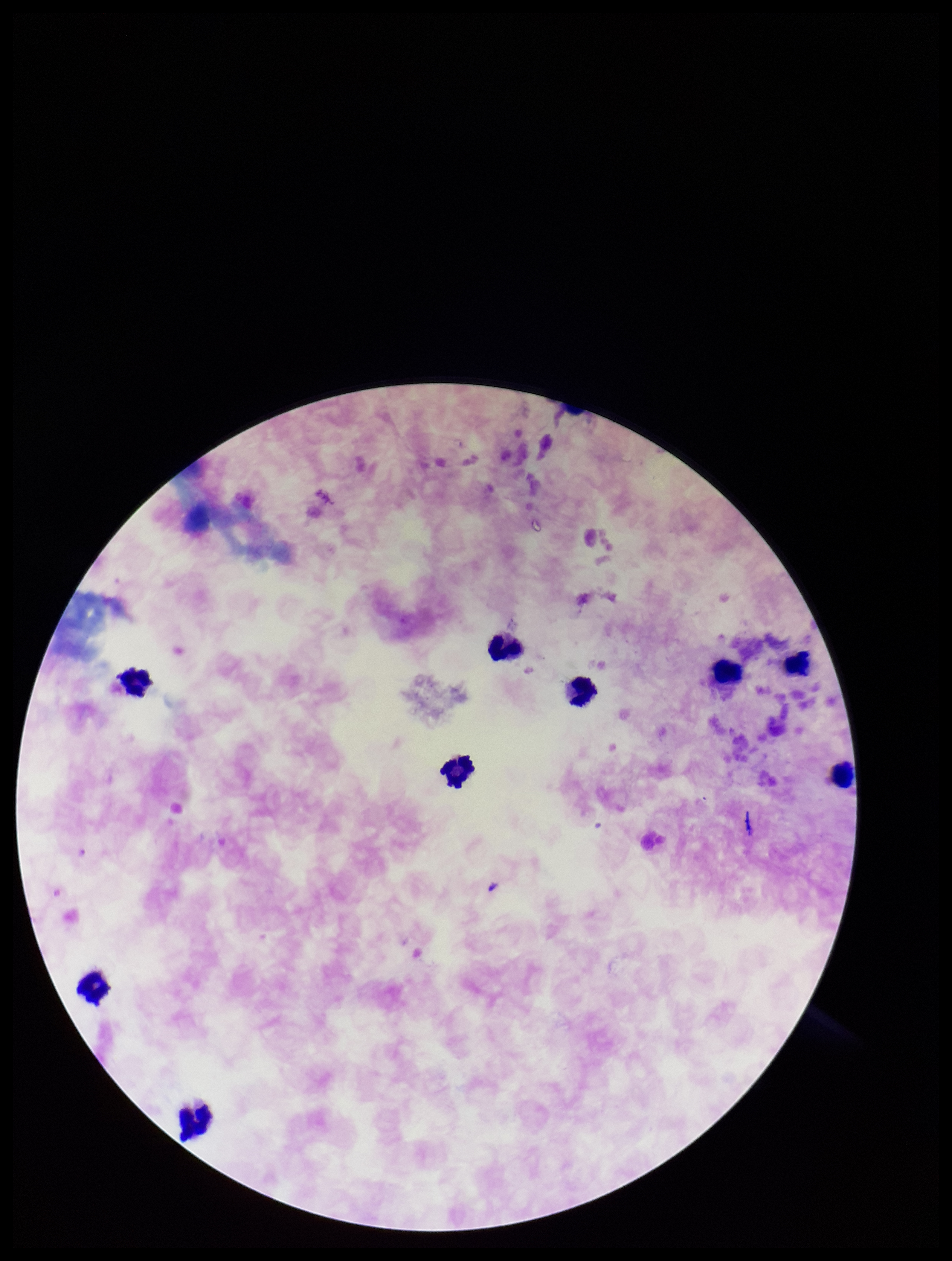

species reported for this patient = Plasmodium falciparum
stain = Giemsa
parasite count = 0
preparation = thick blood smear
image size = 952×1261 pixels
Plasmodium parasites = none identified
patient malaria status = positive
field of view = single
leukocyte count = 9
capture = smartphone photograph through the microscope eyepiece